Locate every malaria parasite.
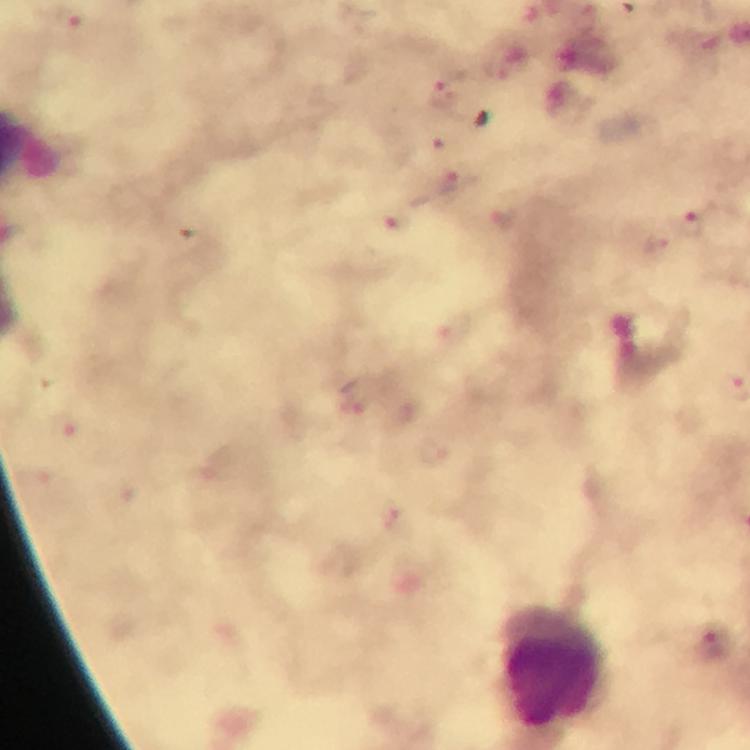
Approximate centers as [x, y] in pixels.
Malaria parasites: [71, 22], [440, 93], [441, 141], [450, 179], [398, 221], [689, 224], [655, 243], [351, 407], [394, 522], [711, 646].

Leukocyte locations: [556, 668]. Thick blood film. A crop from one field of view. Photographed with a smartphone mounted on the microscope. Immersion oil applied. Giemsa stain. At 100x magnification. Image is 750×750 pixels. From a malaria diagnostic workup.